Assess the morphology of the erythrocytes.
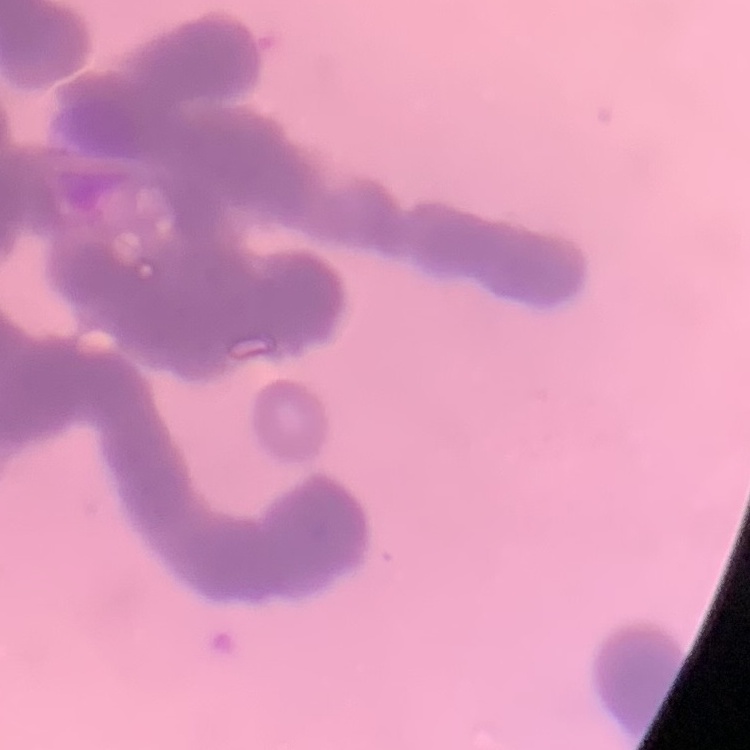
They show rouleaux formation.

Square crop of a larger photomicrograph. Stained with either Field's or Giemsa. Thin blood smear.